Locate platelets.
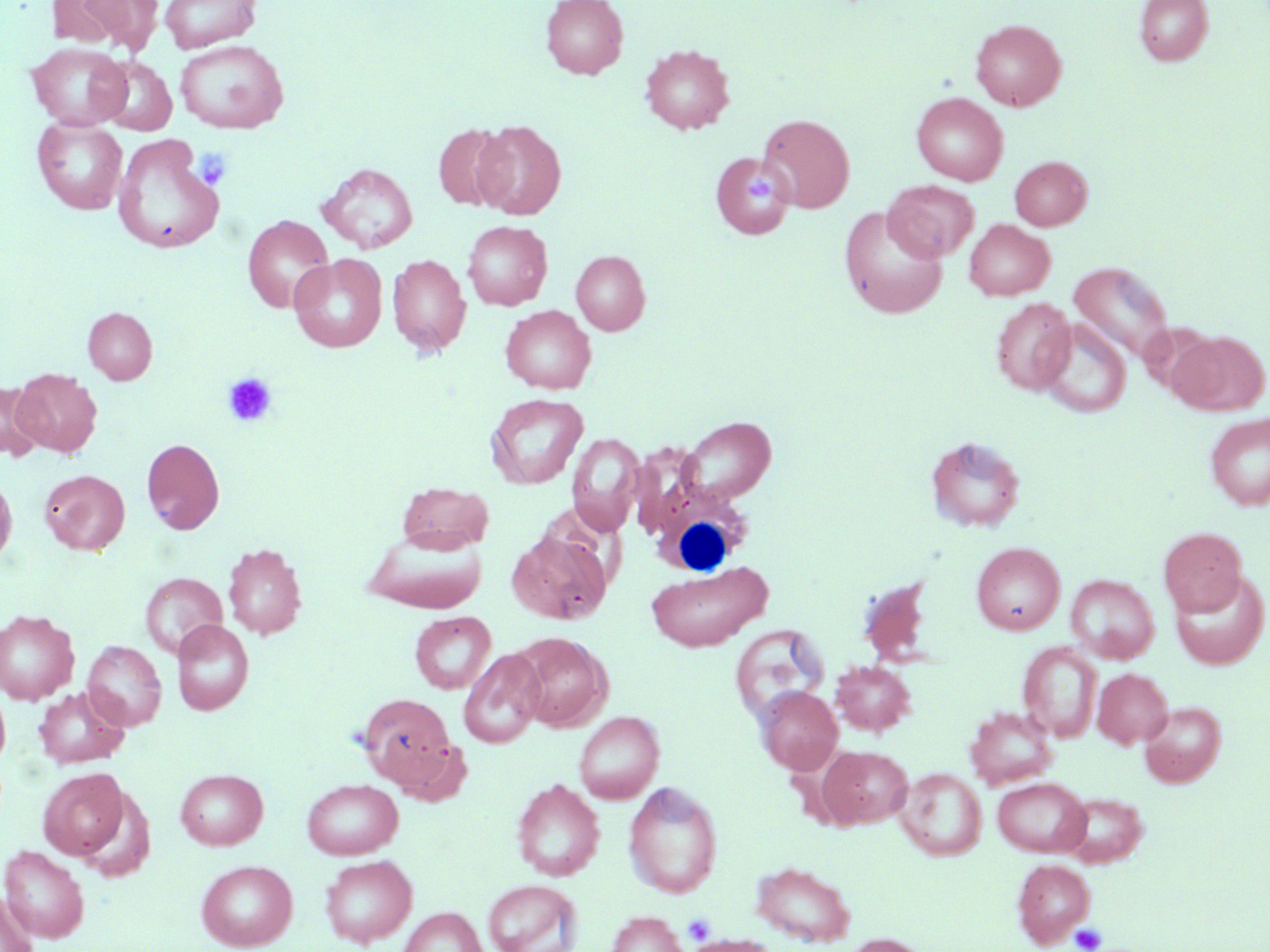
Approximate bounding boxes as (x1,y1)-(x2,y2) corner pairs in pixels.
Platelets: (191,148)-(231,188), (222,373)-(277,427), (683,913)-(715,944), (1069,923)-(1107,952).

Summary:
  - Uninfected red blood cell locations: (76,0)-(164,51), (159,0)-(262,52), (540,0)-(628,79), (1134,0)-(1213,66), (970,19)-(1066,111), (175,39)-(289,134), (25,43)-(131,130), (640,44)-(734,134), (95,56)-(177,135), (912,92)-(1008,185), (757,113)-(855,213), (32,117)-(128,215), (472,120)-(566,219), (433,124)-(511,211), (113,134)-(225,254), (709,151)-(795,241), (1010,156)-(1092,230), (319,163)-(418,254), (884,179)-(979,262), (839,207)-(948,319), (242,215)-(334,313), (964,219)-(1054,300), (462,221)-(552,310), (571,250)-(650,335), (289,253)-(387,352), (388,254)-(471,357), (1069,261)-(1175,364), (991,298)-(1075,395), (501,305)-(596,394), (83,307)-(157,384), (1037,319)-(1131,418), (1169,331)-(1269,415), (11,369)-(102,457), (0,380)-(43,461), (485,393)-(588,489), (1205,412)-(1270,511), (679,416)-(777,505), (567,432)-(645,535), (926,436)-(1026,532), (141,437)-(225,534), (40,469)-(129,555), (0,474)-(17,566), (397,482)-(493,554), (1159,526)-(1247,616), (507,529)-(613,625), (365,530)-(486,614), (971,542)-(1065,635), (223,543)-(307,640), (647,562)-(771,651), (1169,569)-(1270,670), (140,572)-(228,658), (1067,575)-(1159,663), (0,609)-(80,705), (409,611)-(496,694), (171,619)-(253,715), (730,624)-(829,724), (512,633)-(611,731), (83,640)-(167,730), (1018,642)-(1102,743), (458,649)-(545,748), (831,661)-(916,736), (1093,668)-(1172,748), (0,685)-(10,770), (756,686)-(843,774), (33,687)-(129,769), (357,692)-(459,792), (1139,701)-(1226,787), (965,706)-(1057,788), (574,711)-(665,804), (817,744)-(912,828), (38,768)-(129,860), (175,768)-(268,850), (896,769)-(986,861), (993,777)-(1091,856), (302,778)-(403,859), (512,778)-(605,881), (624,781)-(723,898), (1059,791)-(1148,867), (1,844)-(90,943), (320,855)-(417,947), (1012,859)-(1096,947), (196,860)-(298,950), (750,860)-(856,947), (483,879)-(583,952), (1,893)-(39,952), (398,907)-(487,952), (606,911)-(687,952), (841,933)-(934,952), (684,934)-(776,951)
  - White blood cell locations: (649,464)-(756,580)
  - Slide-level diagnosis: no evidence of blood parasites
  - Magnification: 1000x
  - Field of view: one of a larger specimen
  - Preparation: thin blood smear
  - Image size: 1270×952 pixels
  - Stain: May-Grünwald-Giemsa
  - Modality: optical microscopy